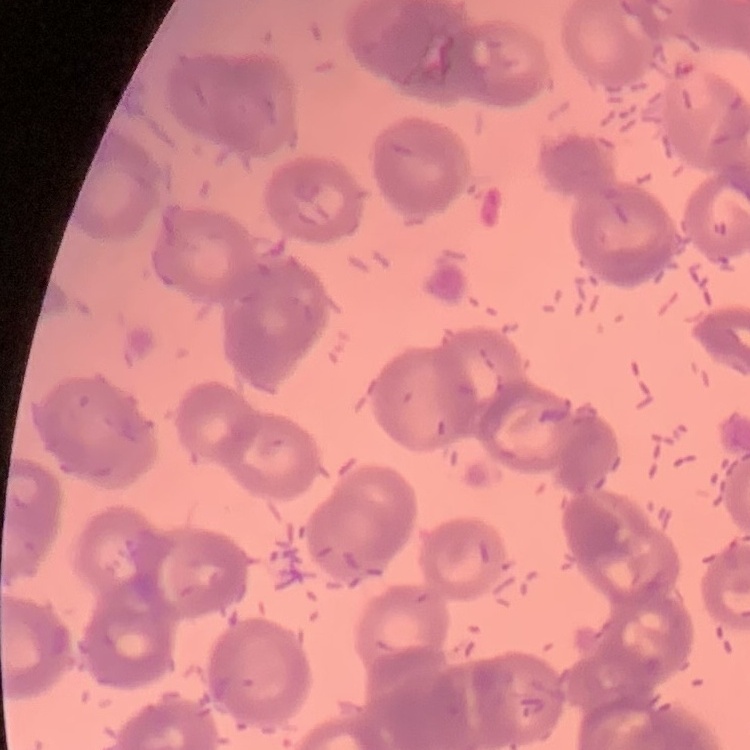
The red blood cells exhibit rouleaux formation. One tile cut from a larger photomicrograph. Stained with either Field's or Giemsa. Thin peripheral smear.